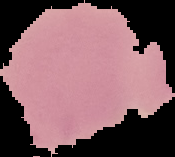

Image is 175×157 pixels. From a thin blood smear. Segmented cell region on a black background. Result: no Plasmodium parasites seen.